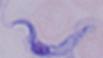
A trypanosome is seen. Captured at 1000x magnification. Micrograph.